Describe the morphology of the erythrocytes.
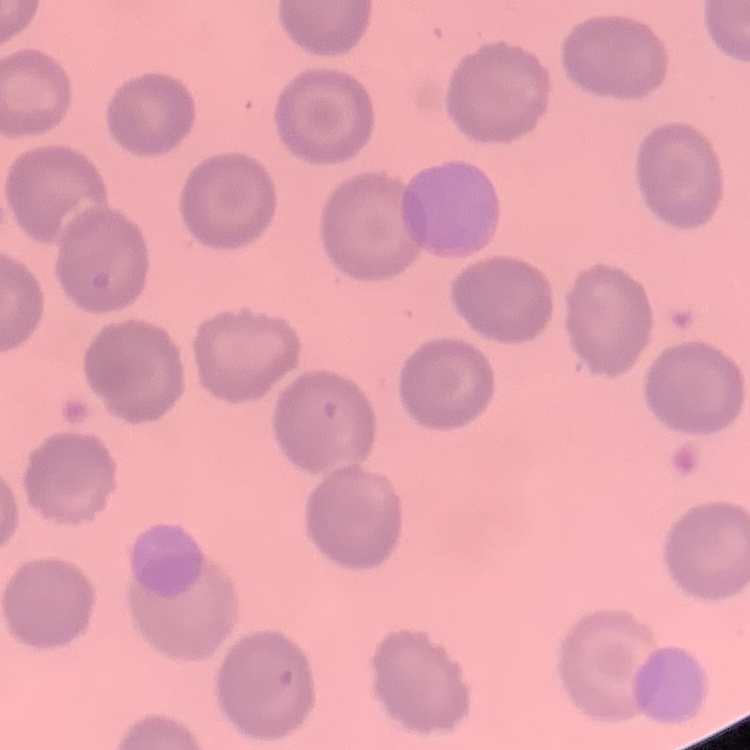

They show no rouleaux formation.

Summary:
  - Image type: square crop of a larger photomicrograph
  - Preparation: thin blood film
  - Stain: Field's or Giemsa